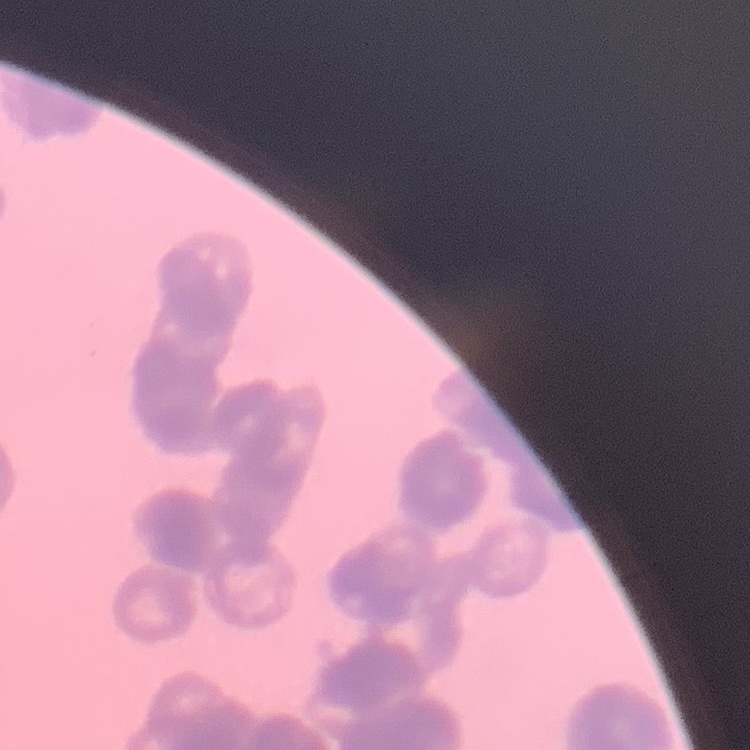 The erythrocytes show rouleaux formation. Square crop of a larger photomicrograph. Stained with either Field's or Giemsa. Thin blood film.